Locate and identify every blood parasite.
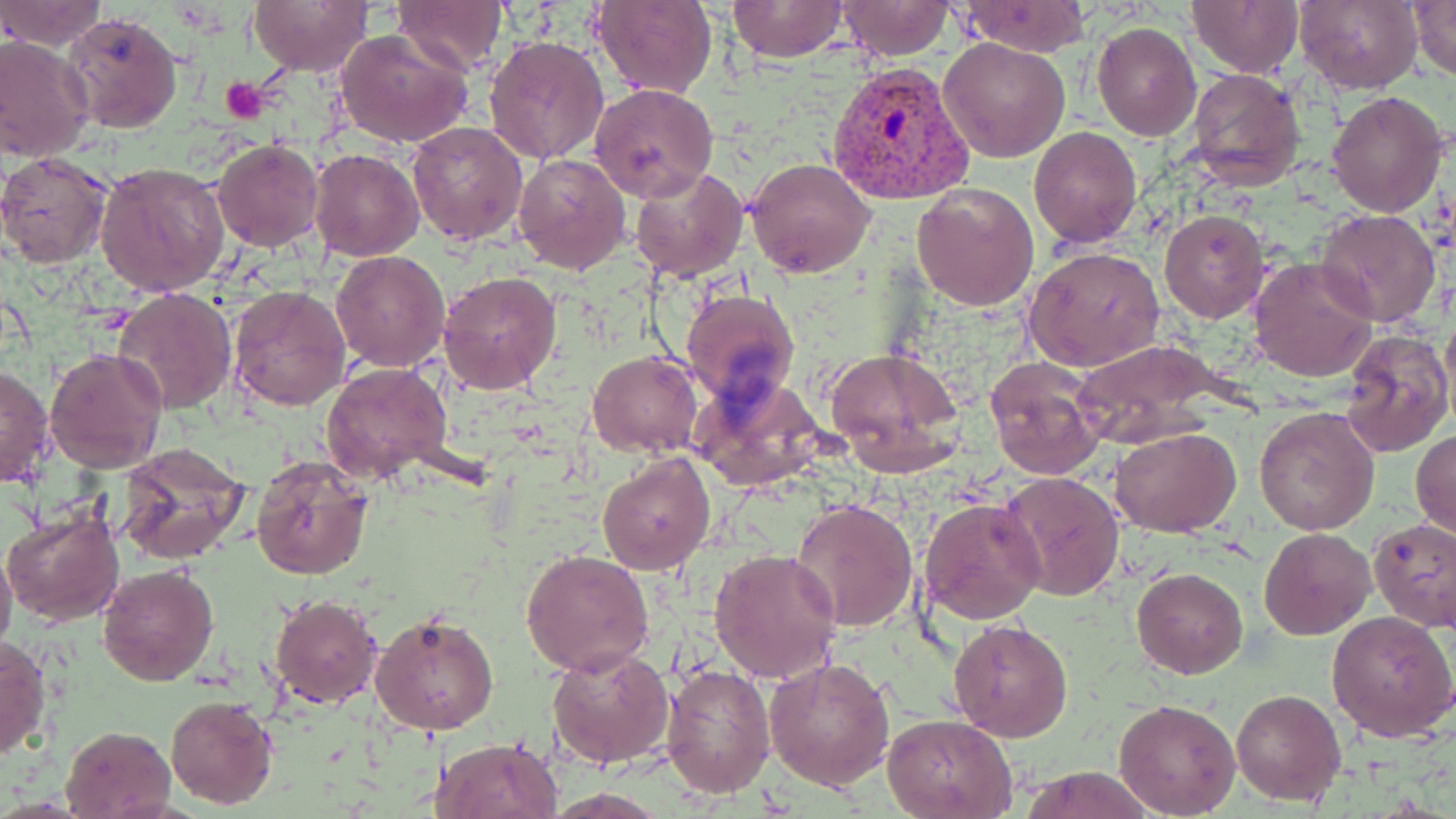

Approximate bounding boxes as (x1, y1, x2, y2) in pixels.
Plasmodium vivax-infected red blood cells: (826, 59, 976, 204).
No Plasmodium falciparum, Plasmodium ovale, Plasmodium malariae, Babesia divergens, or Trypanosoma brucei observed.

slide-level diagnosis = Plasmodium vivax
preparation = thin blood film
stain = May-Grünwald-Giemsa
image size = 1456×819 pixels
platelet locations = approximate bounding boxes as (x1, y1, x2, y2) in pixels: (220, 76, 266, 122)
uninfected red blood cell locations = approximate bounding boxes as (x1, y1, x2, y2) in pixels: (248, 0, 375, 74), (392, 0, 508, 76), (592, 0, 716, 99), (727, 0, 847, 62), (1295, 0, 1422, 94), (1406, 0, 1456, 81), (0, 1, 106, 49), (835, 1, 954, 57), (1188, 1, 1303, 77), (955, 2, 1092, 57), (60, 11, 184, 135), (1091, 22, 1201, 140), (335, 29, 476, 149), (0, 35, 94, 164), (484, 35, 611, 166), (939, 37, 1070, 161), (1185, 68, 1305, 190), (589, 83, 718, 203), (1326, 90, 1449, 216), (406, 120, 528, 245), (1028, 126, 1141, 247), (211, 139, 324, 252), (311, 149, 424, 261), (0, 152, 113, 268), (514, 153, 632, 274), (745, 156, 876, 278), (96, 162, 230, 296), (628, 165, 747, 282), (911, 184, 1039, 311), (1314, 209, 1443, 330), (1159, 210, 1269, 323), (1024, 245, 1165, 372), (332, 251, 449, 371), (1249, 257, 1378, 383), (437, 269, 563, 395), (226, 284, 351, 412), (113, 286, 238, 412), (681, 288, 799, 405), (1340, 328, 1454, 458), (1068, 339, 1231, 447), (43, 346, 167, 473), (823, 346, 966, 478), (587, 351, 702, 458), (984, 357, 1105, 479), (321, 361, 453, 484), (1, 362, 55, 489), (689, 373, 826, 492), (1255, 406, 1380, 537), (1111, 427, 1241, 536), (1412, 428, 1455, 543), (114, 446, 252, 568), (597, 450, 715, 574), (250, 460, 374, 582), (999, 472, 1125, 602), (791, 498, 919, 634), (918, 498, 1045, 625), (3, 509, 123, 626), (1368, 516, 1456, 630), (1259, 528, 1375, 638), (0, 542, 16, 662), (710, 549, 842, 683), (520, 550, 654, 678), (97, 563, 219, 684), (1131, 567, 1248, 679), (269, 594, 381, 709), (369, 610, 499, 736), (1326, 610, 1456, 744), (947, 617, 1074, 741), (1, 635, 51, 763), (546, 645, 676, 768), (764, 657, 896, 791), (660, 663, 776, 799), (1231, 688, 1346, 805), (166, 694, 278, 809), (1113, 698, 1241, 817), (886, 714, 1018, 819), (60, 724, 178, 818), (434, 736, 562, 819), (1015, 766, 1161, 819)
magnification = 1000x
modality = light microscopy
field of view = one of a larger specimen